Assess this cell for malaria.
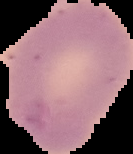

Uninfected.

preparation = thin blood film
image size = 133×154 pixels
image type = segmented cell region with the area outside set to black